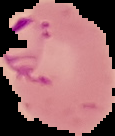
preparation = thin blood film
image type = segmented cell region on a black background
result = Plasmodium parasites identified
image size = 115×136 pixels